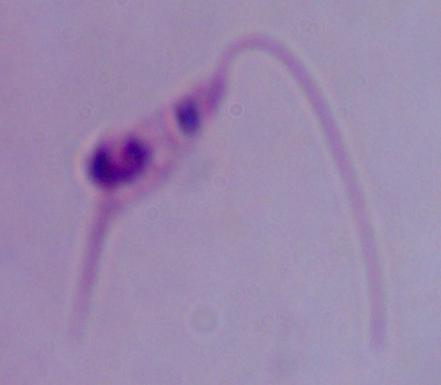
1000x magnification. Photomicrograph. A Leishmania parasite is shown.